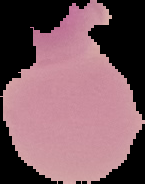
Summary:
  - Image type: segmented cell region with the area outside set to black
  - Result: no Plasmodium parasites detected
  - Image size: 145×184 pixels
  - Preparation: thin blood smear